Outline each uninfected red blood cell.
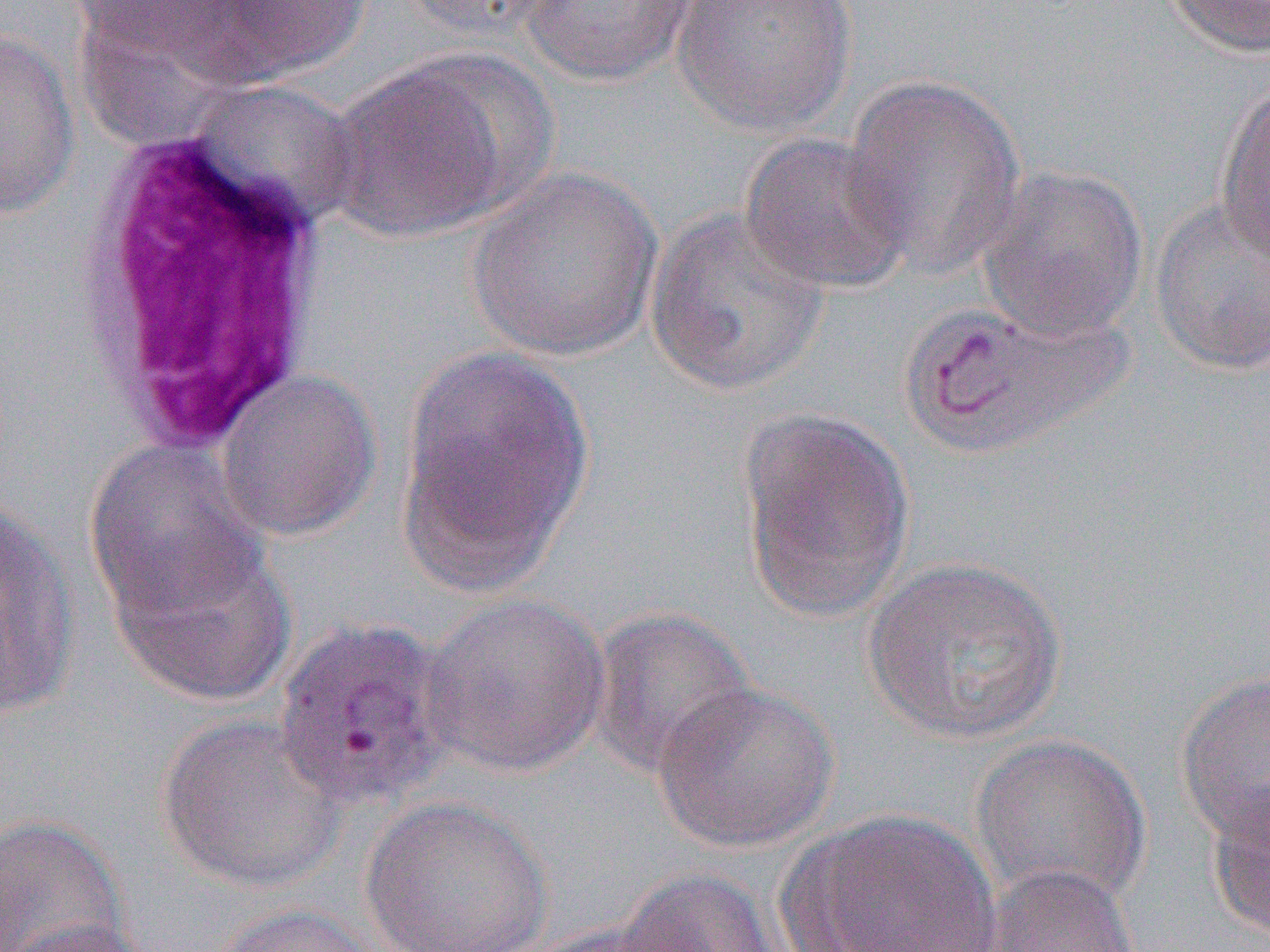
Approximate bounding boxes as named x1/y1/x2/y2 corners in pixels.
Uninfected red blood cells: (x1=188, y1=0, x2=375, y2=83), (x1=399, y1=0, x2=569, y2=43), (x1=519, y1=0, x2=699, y2=86), (x1=670, y1=0, x2=860, y2=139), (x1=1162, y1=0, x2=1270, y2=59), (x1=67, y1=1, x2=273, y2=66), (x1=0, y1=26, x2=81, y2=220), (x1=323, y1=59, x2=525, y2=243), (x1=841, y1=74, x2=1027, y2=278), (x1=1215, y1=81, x2=1270, y2=265), (x1=738, y1=132, x2=916, y2=296), (x1=467, y1=165, x2=664, y2=362), (x1=977, y1=165, x2=1149, y2=342), (x1=1148, y1=196, x2=1269, y2=376), (x1=644, y1=207, x2=831, y2=399), (x1=909, y1=297, x2=1124, y2=460), (x1=398, y1=348, x2=594, y2=590), (x1=214, y1=370, x2=382, y2=543), (x1=734, y1=406, x2=916, y2=626), (x1=84, y1=441, x2=267, y2=621), (x1=1, y1=504, x2=82, y2=719), (x1=105, y1=530, x2=298, y2=708), (x1=861, y1=554, x2=1069, y2=747), (x1=420, y1=593, x2=610, y2=778), (x1=587, y1=606, x2=758, y2=779), (x1=1174, y1=669, x2=1270, y2=846), (x1=653, y1=680, x2=841, y2=853), (x1=155, y1=714, x2=348, y2=892), (x1=970, y1=734, x2=1153, y2=909), (x1=1206, y1=789, x2=1270, y2=941), (x1=360, y1=797, x2=555, y2=952), (x1=792, y1=808, x2=1005, y2=951), (x1=0, y1=813, x2=130, y2=952), (x1=984, y1=862, x2=1137, y2=951), (x1=611, y1=867, x2=783, y2=952), (x1=208, y1=903, x2=387, y2=952), (x1=3, y1=918, x2=158, y2=952), (x1=521, y1=920, x2=696, y2=951).

Summary:
  - White blood cell locations: (x1=65, y1=125, x2=344, y2=454)
  - Slide-level diagnosis: Plasmodium vivax
  - Image size: 1270×952 pixels
  - Magnification: 1000x
  - Preparation: thin blood film
  - Field of view: one of a larger specimen
  - Modality: light microscopy